Identify the parasite.
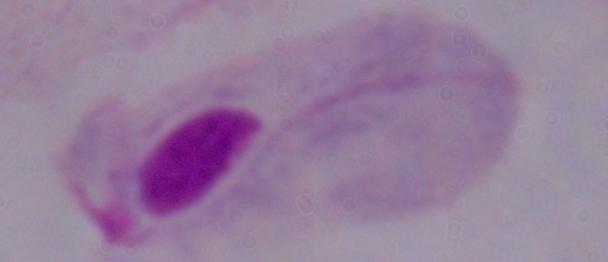
A trichomonad.

1000x magnification. Micrograph.